Identify the blood parasite species.
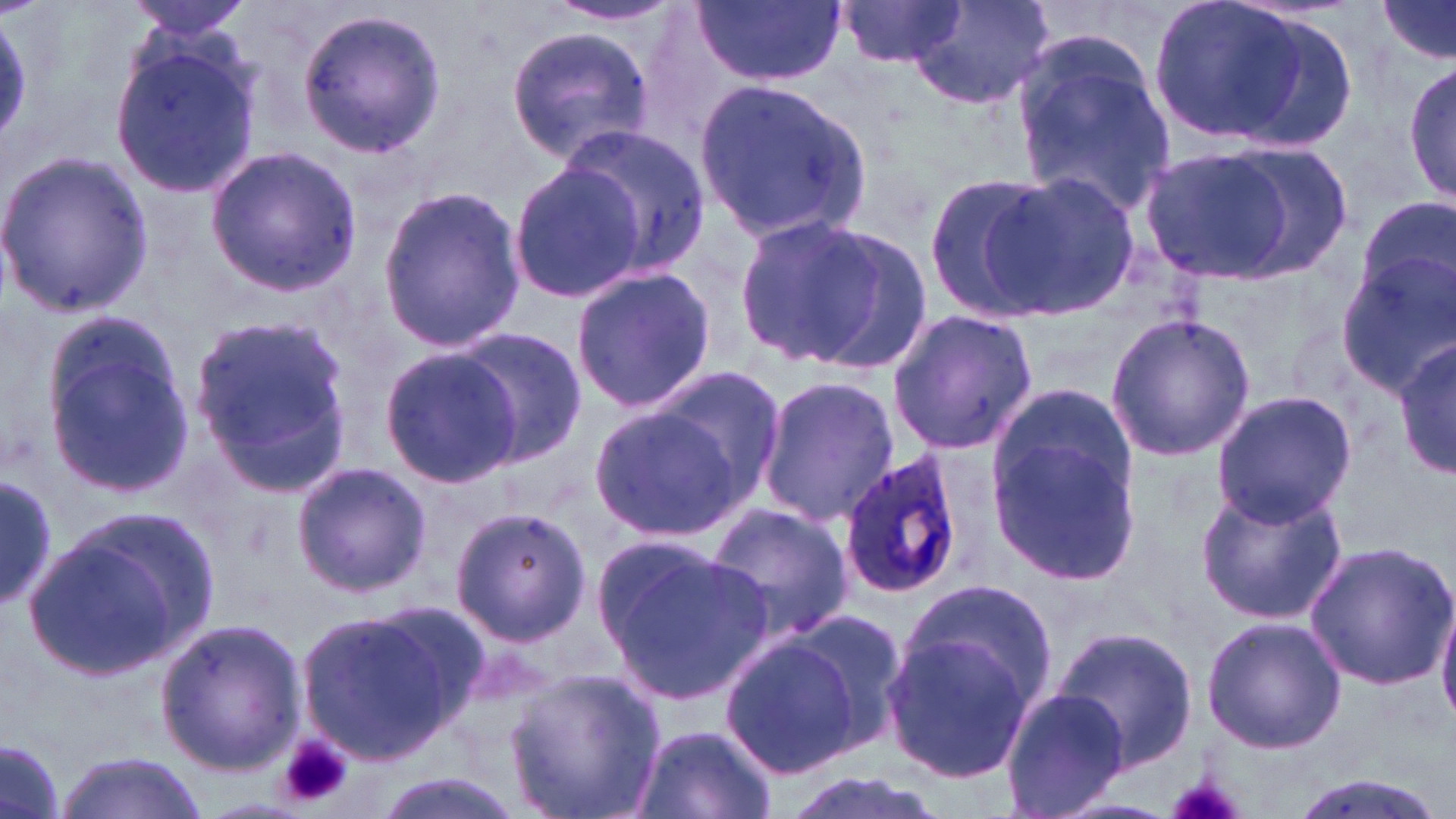
Plasmodium ovale.

Approximate bounding boxes as (x1, y1, x2, y2) in pixels. Plasmodium ovale-infected red blood cell locations: (835, 449, 967, 601). Uninfected red blood cell locations: (126, 0, 259, 41), (695, 0, 846, 87), (835, 0, 966, 71), (906, 0, 1055, 111), (1144, 0, 1318, 148), (1372, 0, 1455, 68), (543, 2, 686, 27), (297, 6, 446, 159), (505, 22, 656, 167), (106, 31, 265, 204), (1012, 35, 1177, 219), (1404, 54, 1456, 210), (695, 76, 869, 241), (557, 125, 709, 279), (1135, 144, 1319, 286), (206, 146, 363, 296), (0, 151, 155, 318), (507, 165, 639, 304), (921, 170, 1057, 320), (983, 170, 1140, 319), (374, 183, 525, 354), (1356, 195, 1456, 307), (737, 214, 918, 372), (1338, 254, 1455, 395), (570, 265, 717, 416), (885, 308, 1039, 454), (1104, 311, 1255, 461), (191, 314, 350, 483), (41, 326, 193, 499), (448, 327, 587, 467), (1393, 336, 1455, 479), (378, 347, 522, 486), (649, 370, 787, 503), (758, 377, 900, 528), (988, 382, 1135, 515), (1210, 390, 1356, 525), (589, 406, 745, 542), (990, 439, 1138, 581), (292, 460, 430, 596), (0, 475, 60, 610), (1194, 480, 1350, 629), (706, 502, 853, 644), (448, 505, 591, 650), (19, 511, 218, 682), (595, 535, 777, 710), (1303, 540, 1456, 691), (895, 577, 1057, 720), (1435, 593, 1456, 728), (295, 606, 474, 767), (779, 607, 913, 759), (1201, 615, 1347, 753), (156, 617, 307, 774), (1048, 623, 1199, 774), (882, 630, 1035, 783), (718, 632, 866, 779), (503, 666, 666, 819), (1001, 687, 1131, 818), (629, 724, 776, 819), (1, 738, 67, 819), (55, 752, 202, 818), (774, 769, 954, 819), (369, 773, 527, 819), (1285, 774, 1448, 819). Platelet locations: (279, 732, 354, 808), (1164, 773, 1251, 819). One field of a larger specimen. Captured at 1000x magnification. Image is 1456×819 pixels. May-Grünwald-Giemsa-stained preparation. Light microscopy. Thin blood smear.